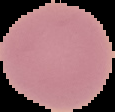

Summary:
  - Image size: 115×112 pixels
  - Result: no malaria parasites seen
  - Preparation: thin blood smear
  - Image type: segmented cell region with the area outside set to black